Report the malaria status of this cell.
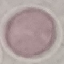

It is uninfected.

Thin smear of blood. Photographed with a smartphone camera at the microscope eyepiece. Automatically extracted cell patch, resized to 64 × 64 pixels. Giemsa-stained preparation.